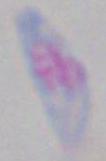
Toxoplasma gondii is seen. Photomicrograph. Captured at 1000x magnification.